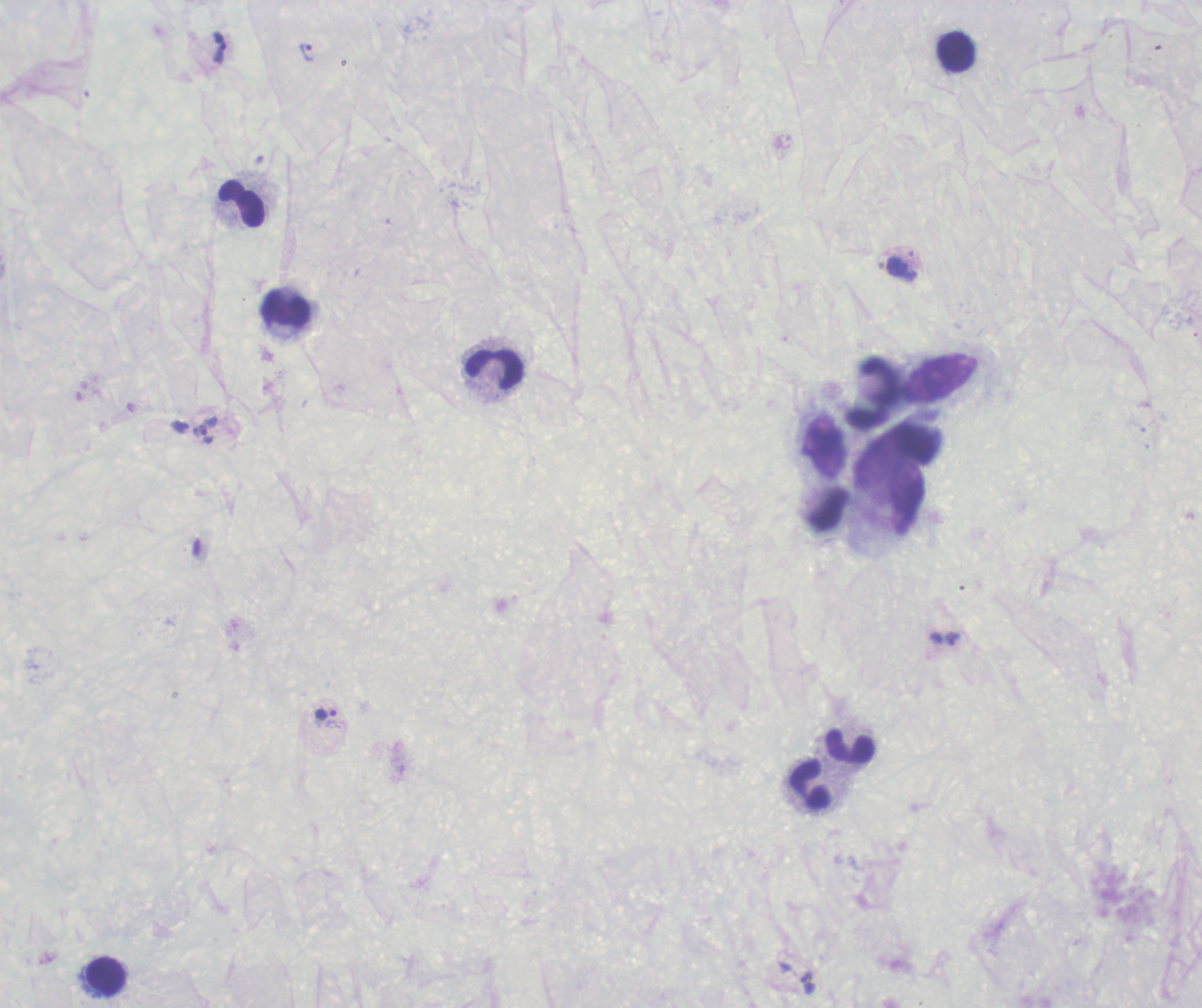
Approximate object centers, in pixels from the top-left corner.
Summary:
  - Trophozoite locations: (x=220, y=48), (x=307, y=52), (x=205, y=429), (x=953, y=638), (x=326, y=714), (x=808, y=983)
  - Leukocyte locations: (x=957, y=52), (x=243, y=204), (x=286, y=308), (x=496, y=369), (x=851, y=745), (x=811, y=784), (x=107, y=975)
  - Magnification: 100x
  - Stain: Romanowsky
  - Coloration quality: bad
  - Context: previously used in a real diagnosis
  - Image size: 1202×1008 pixels
  - Result: Plasmodium parasites detected
  - Field of view: single
  - Preparation: thick smear of blood
  - Background quality: unsatisfactory